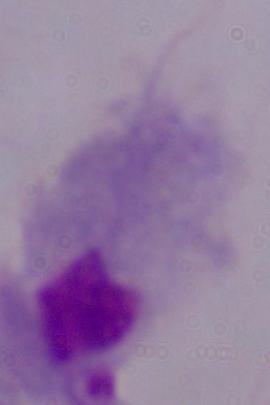

magnification = 1000x
modality = photomicrograph
identification = trichomonad